Comment on the morphology of the red blood cells.
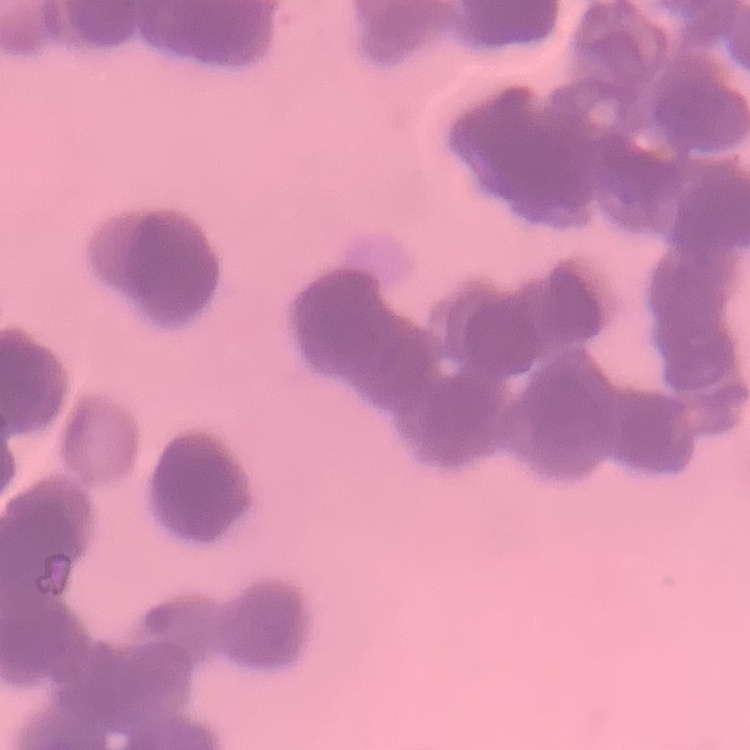

They show rouleaux formation.

Summary:
  - Preparation: thin blood film
  - Image type: one tile cut from a larger photomicrograph
  - Stain: Field's or Giemsa